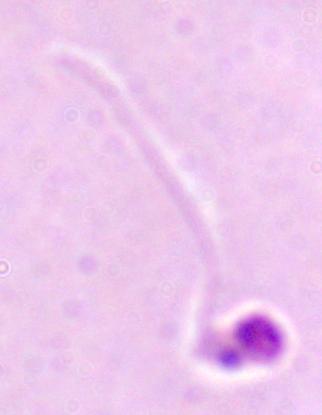

identification = Leishmania
modality = photomicrograph
magnification = 1000x